Identify the parasite.
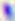

Toxoplasma gondii.

Photomicrograph. Captured at 400x magnification.